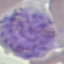

result = malaria parasites detected
preparation = thin smear
capture = smartphone through the microscope eyepiece
stain = Giemsa
image type = cell patch, automatically extracted from a larger field of view and resized to 64 × 64 pixels